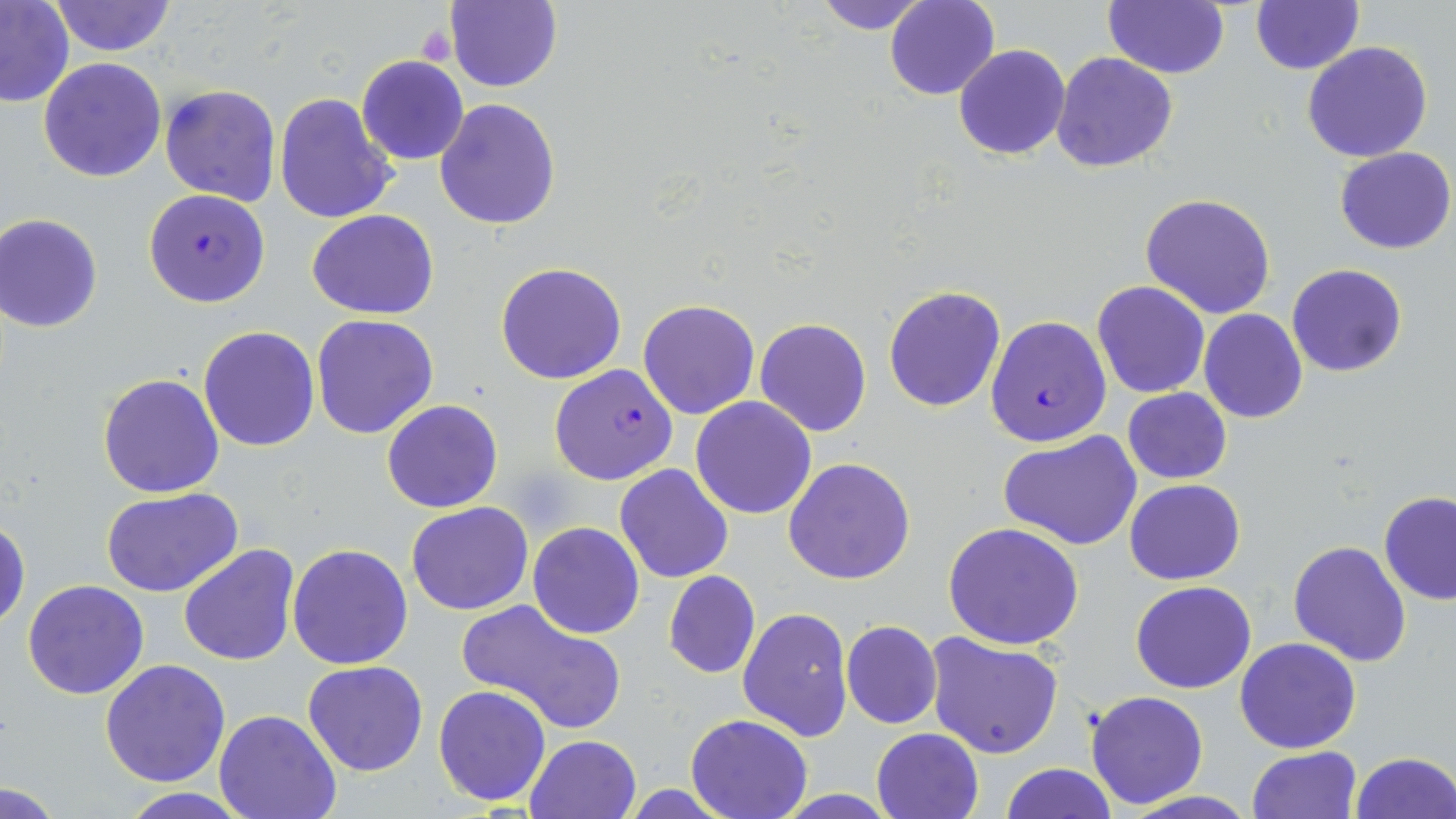
Approximate bounding boxes as named x1/y1/x2/y2 corners in pixels. Platelet locations: (x1=417, y1=24, x2=458, y2=67). Uninfected red blood cell locations: (x1=447, y1=0, x2=563, y2=93), (x1=810, y1=0, x2=932, y2=34), (x1=884, y1=0, x2=999, y2=101), (x1=1104, y1=0, x2=1229, y2=79), (x1=1250, y1=0, x2=1364, y2=75), (x1=0, y1=1, x2=75, y2=108), (x1=50, y1=1, x2=177, y2=56), (x1=1302, y1=40, x2=1433, y2=163), (x1=954, y1=45, x2=1071, y2=161), (x1=1051, y1=50, x2=1179, y2=173), (x1=357, y1=55, x2=469, y2=165), (x1=38, y1=57, x2=167, y2=182), (x1=159, y1=84, x2=281, y2=207), (x1=275, y1=94, x2=399, y2=225), (x1=433, y1=98, x2=561, y2=231), (x1=1334, y1=146, x2=1454, y2=254), (x1=1139, y1=193, x2=1278, y2=319), (x1=307, y1=209, x2=440, y2=319), (x1=1, y1=214, x2=103, y2=332), (x1=496, y1=261, x2=627, y2=386), (x1=1286, y1=263, x2=1407, y2=378), (x1=1092, y1=281, x2=1210, y2=398), (x1=882, y1=284, x2=1005, y2=412), (x1=637, y1=300, x2=760, y2=419), (x1=1198, y1=309, x2=1308, y2=423), (x1=311, y1=315, x2=439, y2=439), (x1=754, y1=318, x2=873, y2=438), (x1=198, y1=325, x2=320, y2=452), (x1=98, y1=373, x2=225, y2=498), (x1=1122, y1=387, x2=1232, y2=484), (x1=690, y1=397, x2=818, y2=520), (x1=381, y1=399, x2=503, y2=514), (x1=1000, y1=431, x2=1142, y2=551), (x1=783, y1=457, x2=916, y2=586), (x1=614, y1=464, x2=736, y2=583), (x1=1124, y1=479, x2=1247, y2=585), (x1=99, y1=486, x2=245, y2=599), (x1=1378, y1=491, x2=1456, y2=605), (x1=406, y1=501, x2=534, y2=615), (x1=1, y1=516, x2=29, y2=631), (x1=528, y1=521, x2=644, y2=638), (x1=942, y1=522, x2=1084, y2=649), (x1=1288, y1=540, x2=1413, y2=667), (x1=287, y1=543, x2=413, y2=669), (x1=178, y1=544, x2=301, y2=667), (x1=663, y1=570, x2=761, y2=678), (x1=22, y1=579, x2=149, y2=699), (x1=1131, y1=580, x2=1257, y2=694), (x1=460, y1=600, x2=627, y2=731), (x1=738, y1=606, x2=853, y2=743), (x1=840, y1=620, x2=943, y2=729), (x1=925, y1=633, x2=1063, y2=758), (x1=1234, y1=637, x2=1362, y2=753), (x1=101, y1=658, x2=232, y2=787), (x1=302, y1=660, x2=429, y2=777), (x1=432, y1=684, x2=553, y2=806), (x1=1085, y1=690, x2=1209, y2=809), (x1=215, y1=710, x2=342, y2=819), (x1=686, y1=713, x2=814, y2=819), (x1=872, y1=728, x2=984, y2=818), (x1=524, y1=733, x2=642, y2=819), (x1=1247, y1=746, x2=1361, y2=819), (x1=1349, y1=751, x2=1456, y2=819), (x1=1001, y1=763, x2=1117, y2=819), (x1=2, y1=781, x2=64, y2=816), (x1=619, y1=784, x2=741, y2=817), (x1=1117, y1=791, x2=1264, y2=819). Plasmodium falciparum-infected red blood cell locations: (x1=145, y1=187, x2=271, y2=309), (x1=985, y1=315, x2=1111, y2=447), (x1=549, y1=364, x2=679, y2=485). Slide-level diagnosis: Plasmodium falciparum. One field of a larger specimen. Image is 1456×819 pixels. 1000x magnification. May-Grünwald-Giemsa-stained preparation. Thin blood smear. Light microscopy.